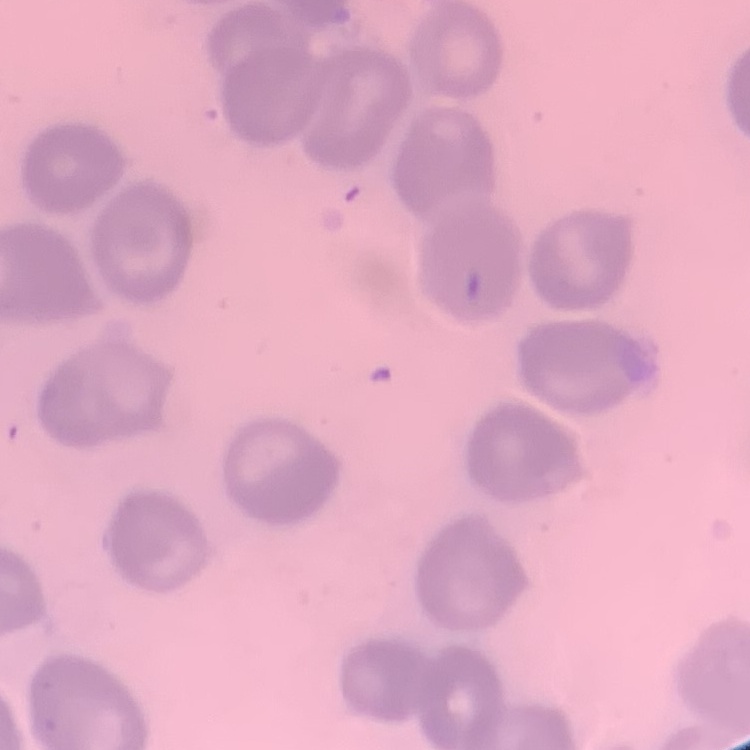
The red blood cells exhibit no rouleaux formation. Thin blood smear. One tile cut from a larger photomicrograph. Stained with either Field's or Giemsa.